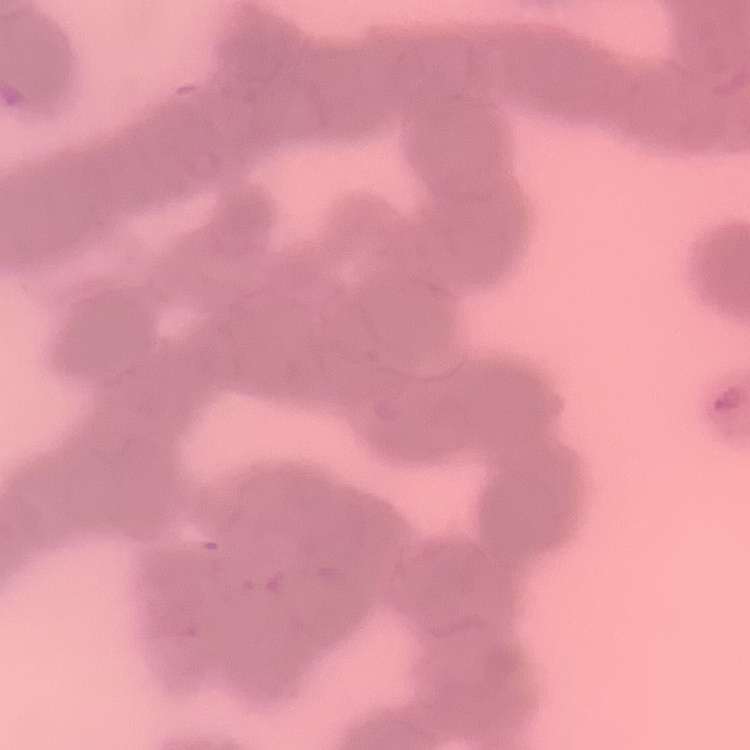
Summary:
  - Erythrocyte morphology: rouleaux formation
  - Stain: Field's or Giemsa
  - Image type: one tile cut from a larger photomicrograph
  - Preparation: thin blood film